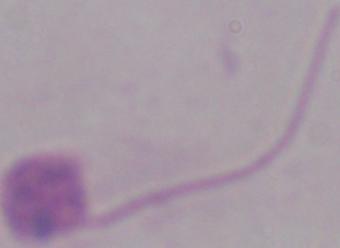
Summary:
  - Magnification: 1000x
  - Identification: Leishmania
  - Modality: micrograph